Name the blood parasite species.
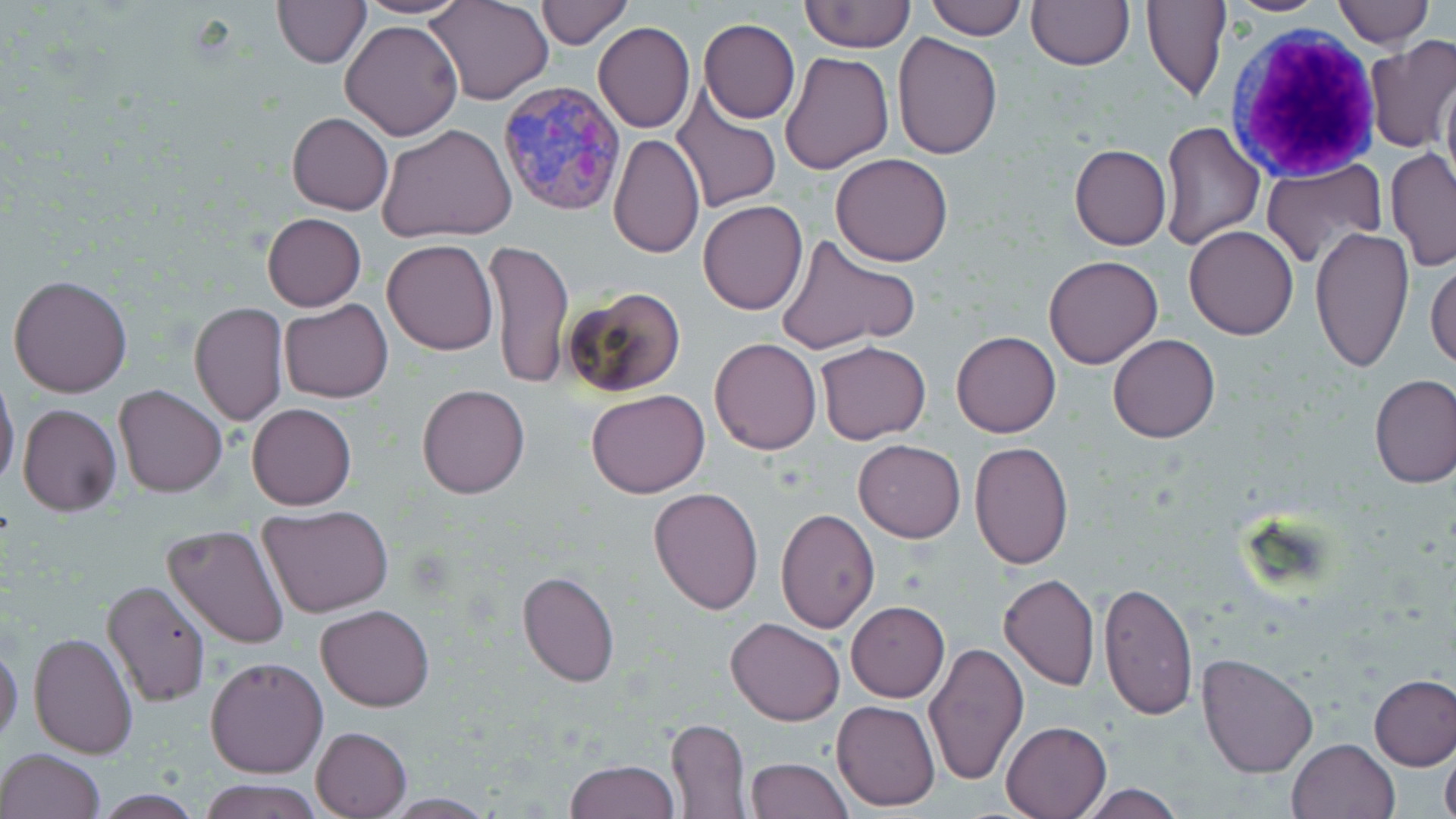

Plasmodium vivax.

Approximate bounding boxes as named x1/y1/x2/y2 corners in pixels. White blood cell locations: (x1=1228, y1=25, x2=1380, y2=179). Uninfected red blood cell locations: (x1=356, y1=0, x2=469, y2=19), (x1=425, y1=0, x2=551, y2=106), (x1=535, y1=0, x2=631, y2=48), (x1=923, y1=0, x2=1027, y2=39), (x1=1222, y1=0, x2=1334, y2=16), (x1=1335, y1=0, x2=1431, y2=46), (x1=273, y1=1, x2=370, y2=67), (x1=799, y1=1, x2=915, y2=52), (x1=1026, y1=1, x2=1134, y2=69), (x1=1141, y1=1, x2=1230, y2=101), (x1=698, y1=18, x2=800, y2=124), (x1=340, y1=19, x2=464, y2=141), (x1=593, y1=22, x2=695, y2=134), (x1=891, y1=32, x2=1002, y2=159), (x1=1365, y1=39, x2=1456, y2=152), (x1=778, y1=49, x2=893, y2=175), (x1=1439, y1=67, x2=1455, y2=197), (x1=669, y1=85, x2=783, y2=214), (x1=287, y1=112, x2=394, y2=215), (x1=1159, y1=121, x2=1264, y2=249), (x1=377, y1=124, x2=516, y2=243), (x1=607, y1=134, x2=705, y2=259), (x1=1069, y1=144, x2=1171, y2=250), (x1=1384, y1=150, x2=1456, y2=271), (x1=831, y1=152, x2=953, y2=268), (x1=1261, y1=160, x2=1386, y2=269), (x1=698, y1=200, x2=808, y2=315), (x1=262, y1=214, x2=366, y2=311), (x1=1310, y1=225, x2=1413, y2=372), (x1=1184, y1=226, x2=1299, y2=340), (x1=773, y1=233, x2=919, y2=356), (x1=485, y1=238, x2=573, y2=392), (x1=382, y1=239, x2=498, y2=356), (x1=1043, y1=255, x2=1162, y2=369), (x1=1426, y1=256, x2=1456, y2=371), (x1=8, y1=274, x2=133, y2=398), (x1=562, y1=285, x2=687, y2=400), (x1=279, y1=300, x2=394, y2=402), (x1=190, y1=302, x2=290, y2=427), (x1=950, y1=331, x2=1061, y2=438), (x1=1108, y1=333, x2=1220, y2=442), (x1=710, y1=337, x2=822, y2=455), (x1=816, y1=339, x2=931, y2=445), (x1=0, y1=372, x2=20, y2=491), (x1=1370, y1=375, x2=1456, y2=487), (x1=114, y1=384, x2=227, y2=497), (x1=416, y1=384, x2=529, y2=499), (x1=585, y1=389, x2=710, y2=497), (x1=18, y1=403, x2=122, y2=516), (x1=247, y1=403, x2=356, y2=511), (x1=853, y1=439, x2=966, y2=542), (x1=970, y1=440, x2=1075, y2=571), (x1=648, y1=488, x2=763, y2=614), (x1=258, y1=504, x2=396, y2=618), (x1=775, y1=507, x2=880, y2=632), (x1=163, y1=525, x2=290, y2=650), (x1=517, y1=571, x2=620, y2=687), (x1=998, y1=574, x2=1100, y2=692), (x1=101, y1=579, x2=210, y2=706), (x1=1098, y1=581, x2=1198, y2=720), (x1=846, y1=601, x2=948, y2=702), (x1=316, y1=604, x2=434, y2=711), (x1=726, y1=617, x2=846, y2=725), (x1=28, y1=631, x2=137, y2=759), (x1=0, y1=640, x2=23, y2=746), (x1=924, y1=641, x2=1028, y2=784), (x1=1197, y1=652, x2=1321, y2=777), (x1=205, y1=656, x2=327, y2=777), (x1=1369, y1=675, x2=1456, y2=771), (x1=832, y1=700, x2=939, y2=811), (x1=666, y1=717, x2=751, y2=819), (x1=1000, y1=720, x2=1112, y2=818), (x1=311, y1=726, x2=412, y2=817), (x1=1286, y1=737, x2=1400, y2=819), (x1=1440, y1=745, x2=1456, y2=819), (x1=0, y1=748, x2=106, y2=819), (x1=745, y1=756, x2=852, y2=819), (x1=564, y1=759, x2=680, y2=818), (x1=201, y1=779, x2=321, y2=819), (x1=1075, y1=782, x2=1186, y2=818), (x1=374, y1=793, x2=499, y2=817). Plasmodium vivax-infected red blood cell locations: (x1=497, y1=78, x2=628, y2=216). Single field of view. Thin blood film. Image is 1456×819 pixels. Captured at 1000x magnification. Light microscopy. May-Grünwald-Giemsa stain.